Identify the parasite.
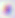

Toxoplasma gondii.

{
  "magnification": "400x",
  "modality": "micrograph"
}